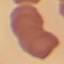

result = no malaria parasites seen
stain = Giemsa
preparation = thin blood smear
image type = automatically extracted cell patch, resized to 64 × 64 pixels
capture = smartphone camera at the microscope eyepiece